Classify this cell by malaria status.
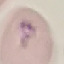

Parasitized.

{
  "stain": "Giemsa",
  "preparation": "thin blood smear",
  "image_type": "automatically extracted cell patch, resized to 64 × 64 pixels",
  "capture": "smartphone through the microscope eyepiece"
}